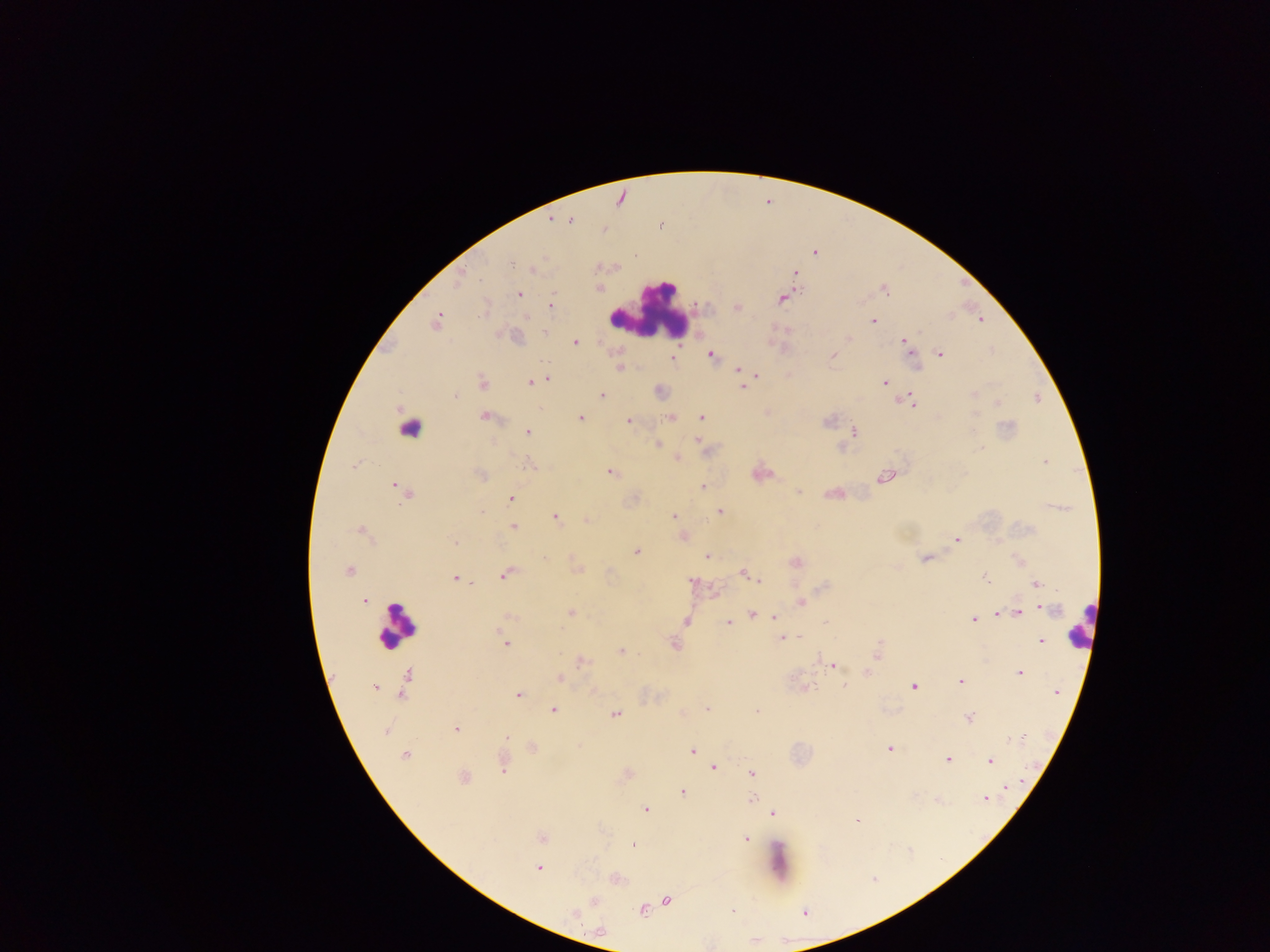
Approximate centers as {x, y} in pixels. Malaria parasite locations: {815, 252}, {510, 262}, {533, 268}, {599, 288}, {519, 295}, {780, 299}, {552, 305}, {737, 307}, {483, 308}, {436, 321}, {873, 321}, {545, 330}, {901, 340}, {576, 343}, {711, 354}, {940, 354}, {620, 367}, {737, 369}, {739, 373}, {757, 375}, {546, 377}, {529, 382}, {483, 383}, {884, 383}, {742, 387}, {601, 393}, {974, 393}, {456, 394}, {910, 398}, {996, 402}, {916, 404}, {703, 416}, {975, 416}, {483, 417}, {671, 417}, {580, 418}, {627, 421}, {528, 431}, {851, 431}, {697, 440}, {658, 444}, {979, 449}, {678, 456}, {1043, 462}, {528, 463}, {354, 464}, {609, 471}, {480, 476}, {883, 478}, {394, 486}, {703, 486}, {799, 491}, {403, 493}, {827, 493}, {513, 499}, {720, 511}, {481, 513}, {673, 516}, {555, 517}, {582, 519}, {586, 519}, {514, 527}, {360, 530}, {684, 535}, {955, 539}, {454, 542}, {638, 551}, {708, 555}, {545, 558}, {923, 558}, {348, 572}, {743, 573}, {504, 574}, {751, 575}, {454, 577}, {986, 578}, {758, 579}, {456, 580}, {693, 582}, {1036, 582}, {365, 599}, {800, 602}, {1040, 607}, {751, 614}, {1020, 614}, {773, 615}, {997, 615}, {509, 617}, {973, 620}, {686, 621}, {726, 623}, {497, 628}, {781, 639}, {1041, 640}, {504, 643}, {674, 646}, {622, 651}, {877, 652}, {580, 661}, {834, 665}, {867, 672}, {1020, 673}, {406, 674}, {559, 677}, {960, 680}, {845, 686}, {807, 687}, {374, 688}, {913, 688}, {1055, 692}, {518, 693}, {402, 695}, {706, 707}, {552, 708}, {756, 709}, {682, 712}, {614, 714}, {968, 718}, {455, 728}, {386, 730}, {506, 736}, {1023, 736}, {578, 745}, {533, 747}, {890, 749}, {693, 752}, {404, 754}, {947, 758}, {989, 762}, {504, 765}, {713, 767}, {752, 773}, {465, 777}, {1007, 789}, {684, 791}, {753, 797}, {986, 801}, {646, 808}, {773, 813}, {857, 821}, {746, 837}, {632, 845}, {536, 868}, {667, 900}, {594, 901}, {642, 910}, {734, 910}. Leukocyte locations: {646, 312}, {411, 425}, {397, 627}. Sample from Ghana. Thick blood film. Mobile-phone photograph taken through the microscope. One field of view. Image is 1270×952 pixels.